Assess the morphology of the red blood cells.
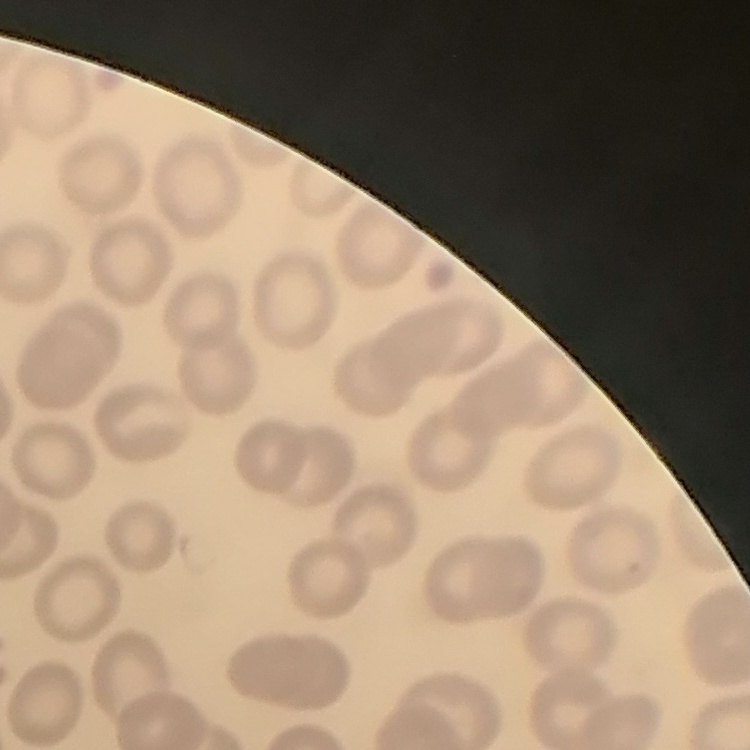
No rouleaux formation.

Summary:
  - Stain: Field's or Giemsa
  - Preparation: thin blood film
  - Image type: square crop of a larger photomicrograph